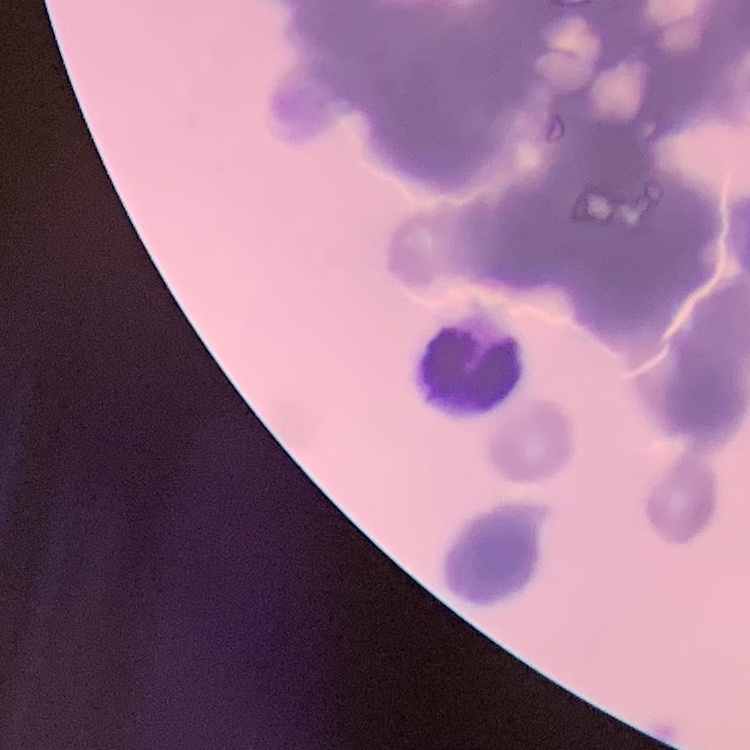

red blood cell morphology = rouleaux formation
stain = Field's or Giemsa
image type = square crop of a larger photomicrograph
preparation = thin peripheral smear